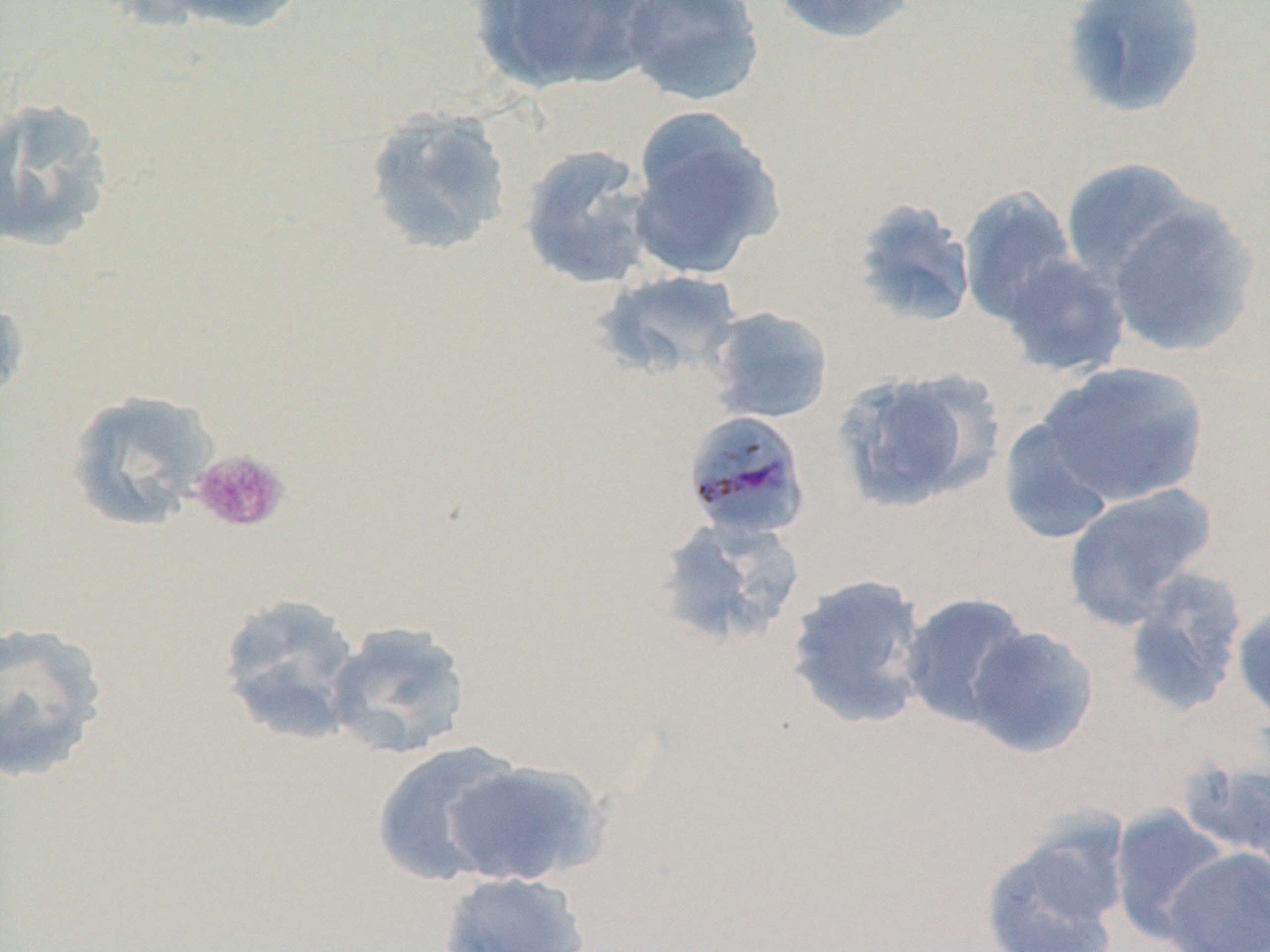

Approximate bounding boxes as (x1,y1)-(x2,y2) corner pairs in pixels. Platelet locations: (190,449)-(290,533). Plasmodium malariae-infected red blood cell locations: (682,410)-(812,541). Uninfected red blood cell locations: (131,0)-(310,34), (470,0)-(655,93), (619,0)-(766,107), (772,0)-(919,45), (1060,0)-(1208,119), (0,96)-(117,253), (363,105)-(514,257), (626,109)-(785,280), (518,143)-(658,290), (1060,158)-(1201,284), (958,186)-(1078,325), (851,198)-(977,329), (1106,200)-(1261,359), (1000,253)-(1131,378), (593,269)-(744,385), (0,274)-(31,410), (706,306)-(834,424), (1035,361)-(1209,507), (831,367)-(1002,513), (65,389)-(220,531), (998,417)-(1116,544), (1062,483)-(1217,629), (656,517)-(806,649), (1121,568)-(1248,717), (785,573)-(931,729), (899,591)-(1034,728), (215,593)-(365,746), (1231,598)-(1270,728), (324,621)-(472,760), (0,622)-(110,784), (964,624)-(1100,759), (370,741)-(526,886), (1184,756)-(1270,872), (443,758)-(606,887), (1109,805)-(1230,943), (979,823)-(1128,952), (1161,846)-(1270,952), (438,871)-(591,952). Slide-level diagnosis: Plasmodium malariae. Light microscopy. One field of a larger specimen. 1000x magnification. Thin blood smear. Image is 1270×952 pixels. May-Grünwald-Giemsa stain.